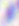 400x magnification. Micrograph. Toxoplasma gondii is seen.